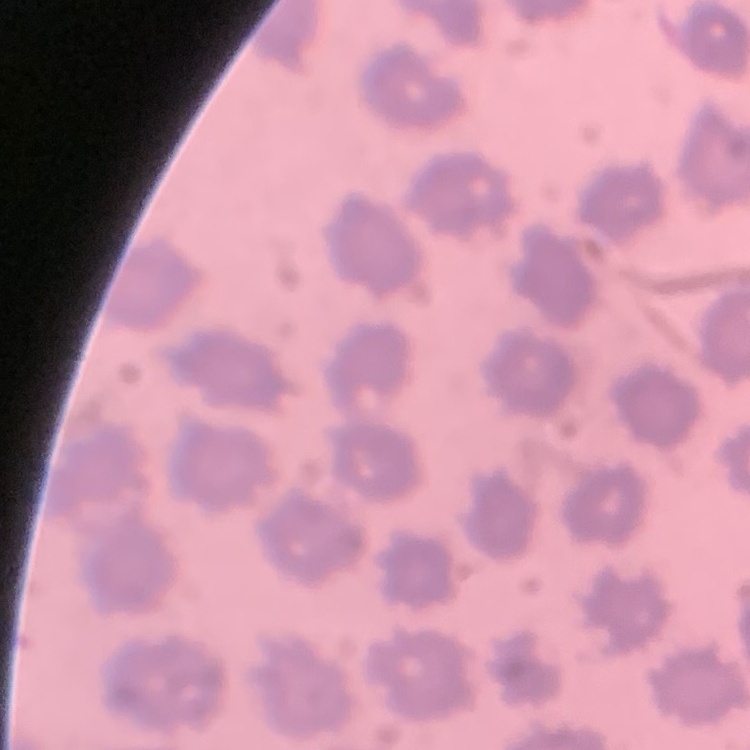
{
  "red_blood_cell_morphology": "no rouleaux formation",
  "image_type": "square crop of a larger photomicrograph",
  "stain": "Field's or Giemsa",
  "preparation": "thin peripheral smear"
}